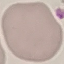
Summary:
  - Malaria status: uninfected
  - Stain: Giemsa
  - Capture: smartphone through the microscope eyepiece
  - Preparation: thin blood film
  - Image type: automatically extracted cell patch, resized to 64 × 64 pixels